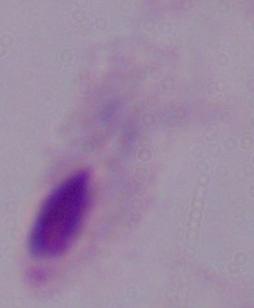

magnification = 1000x
identification = trichomonad
modality = photomicrograph